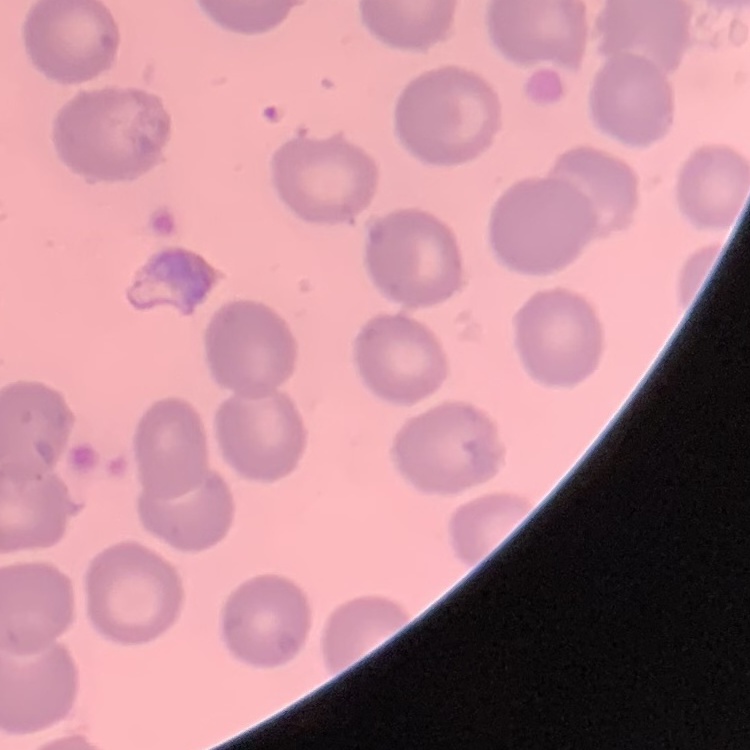
Summary:
  - Erythrocyte morphology: no rouleaux formation
  - Preparation: thin blood film
  - Stain: Field's or Giemsa
  - Image type: one tile cut from a larger photomicrograph